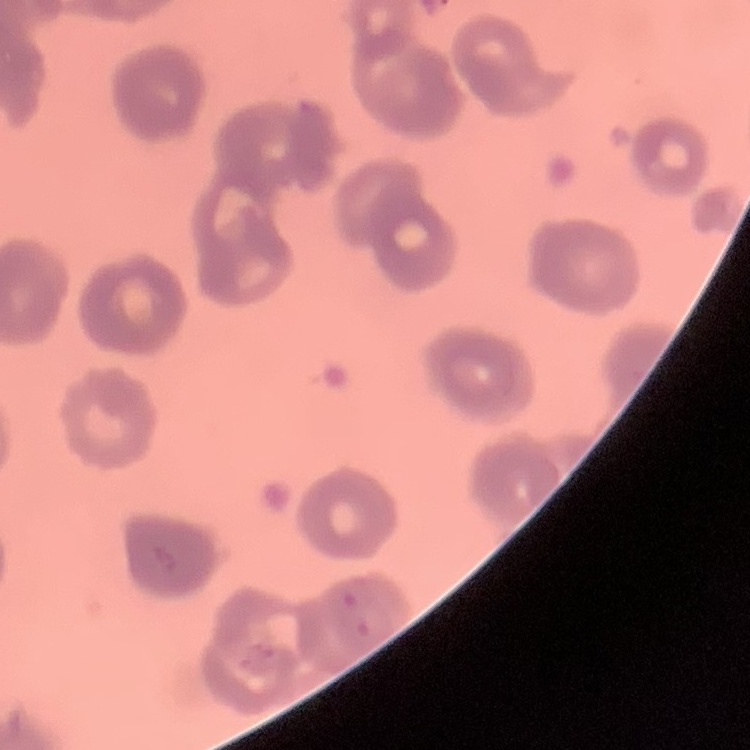
The erythrocytes exhibit rouleaux formation. Thin blood smear. Square crop of a larger photomicrograph. Stained with either Field's or Giemsa.